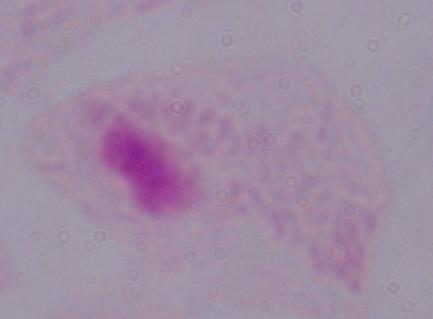

Summary:
  - Modality: micrograph
  - Magnification: 1000x
  - Identification: trichomonad